Comment on the morphology of the erythrocytes.
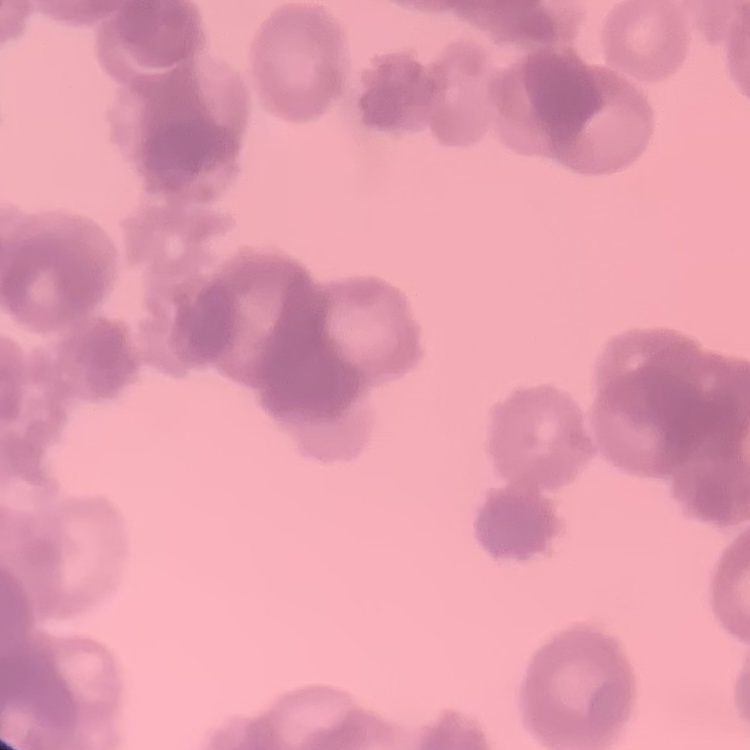

Rouleaux formation.

Thin blood film. Field's or Giemsa stain. Square crop of a larger photomicrograph.